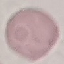

result: no malaria parasites seen
stain: Giemsa
capture: smartphone camera at the microscope eyepiece
preparation: thin smear
image_type: cell patch, automatically extracted from a larger field of view and resized to 64 × 64 pixels